Classify this cell by malaria status.
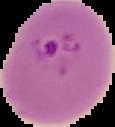

Parasitized.

The area outside the segmented cell region is set to black. From a thin blood film. Image is 115×127 pixels.